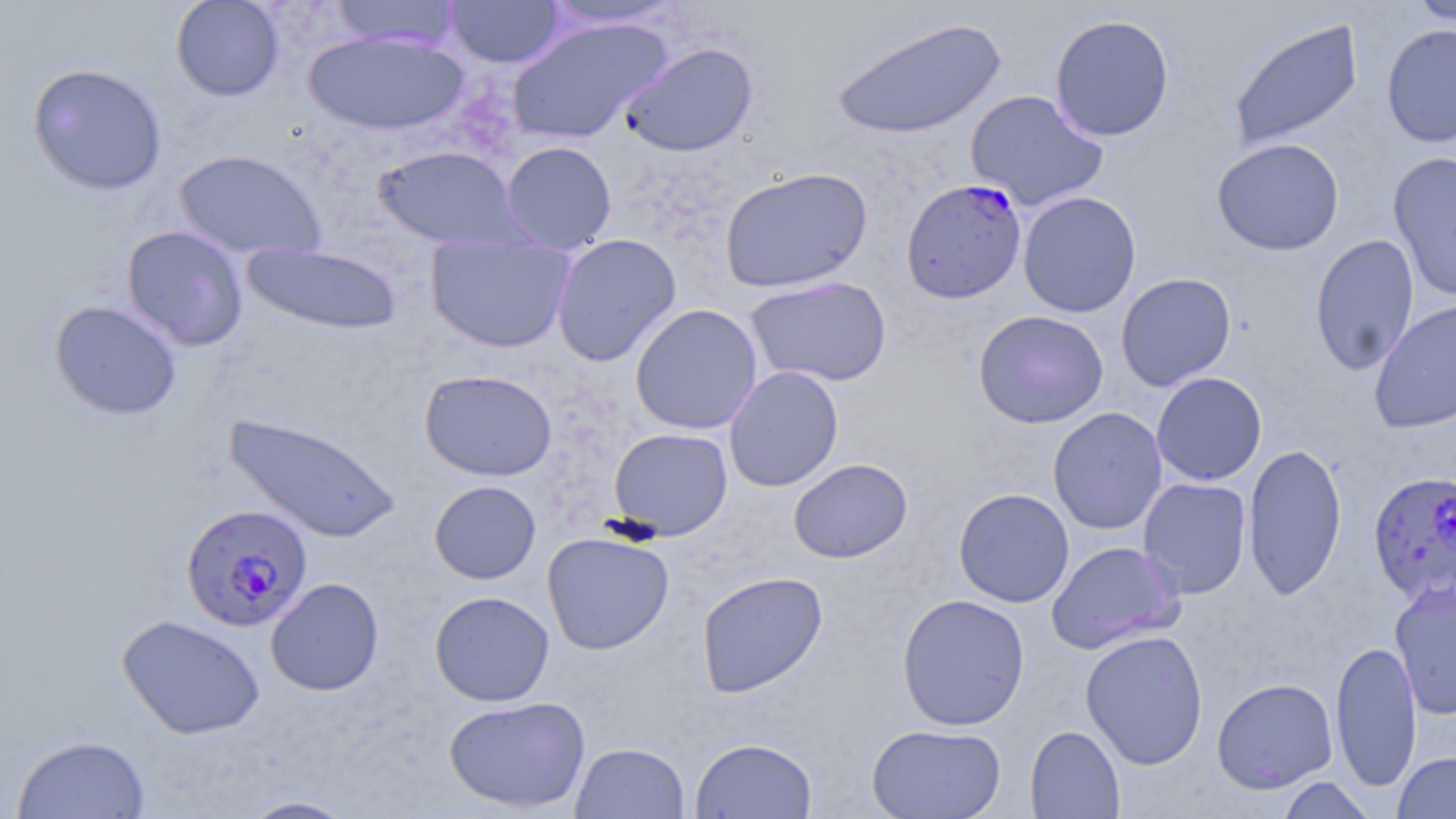

Approximate bounding boxes as [x1, y1, x2, y2] in pixels. Plasmodium falciparum-infected red blood cell locations: [901, 177, 1028, 305], [1367, 470, 1455, 607], [181, 503, 313, 633]. Uninfected red blood cell locations: [170, 0, 285, 102], [330, 0, 461, 51], [445, 0, 564, 68], [1406, 0, 1456, 25], [540, 1, 684, 30], [1049, 13, 1175, 142], [832, 16, 1006, 140], [506, 17, 673, 145], [1228, 18, 1364, 151], [1381, 23, 1456, 148], [304, 31, 469, 136], [619, 41, 759, 158], [27, 62, 167, 196], [965, 89, 1108, 211], [1211, 137, 1344, 256], [501, 140, 617, 254], [372, 144, 526, 251], [173, 149, 326, 260], [1388, 151, 1456, 302], [718, 166, 872, 293], [1018, 191, 1142, 318], [121, 225, 249, 351], [425, 233, 576, 353], [552, 233, 682, 366], [1310, 233, 1420, 376], [241, 243, 402, 335], [1116, 272, 1236, 391], [745, 275, 892, 388], [48, 299, 183, 421], [1368, 299, 1456, 433], [630, 304, 762, 434], [974, 309, 1109, 429], [723, 366, 843, 492], [419, 369, 557, 481], [1151, 371, 1267, 486], [1048, 407, 1167, 535], [223, 412, 404, 544], [608, 427, 733, 540], [1242, 443, 1347, 601], [788, 458, 912, 563], [1137, 477, 1252, 598], [429, 480, 541, 584], [953, 488, 1074, 607], [542, 531, 674, 654], [1046, 540, 1183, 654], [697, 571, 828, 697], [265, 577, 384, 696], [1389, 579, 1456, 720], [429, 590, 554, 706], [897, 593, 1030, 730], [116, 614, 265, 739], [1080, 630, 1208, 768], [1330, 638, 1422, 793], [1212, 678, 1338, 794], [443, 695, 590, 814], [867, 723, 1006, 818], [1025, 726, 1125, 819], [11, 733, 151, 819], [689, 738, 817, 819], [570, 742, 690, 818], [1392, 751, 1456, 818], [1275, 775, 1378, 819], [238, 795, 359, 818]. Slide-level diagnosis: Plasmodium falciparum. Optical microscopy. Single field of view. 1000x magnification. Thin blood film. Image is 1456×819 pixels. May-Grünwald-Giemsa stain.